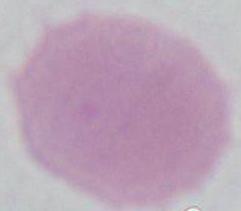
Captured at 1000x magnification. A red blood cell is seen. Micrograph.